Identify the parasite.
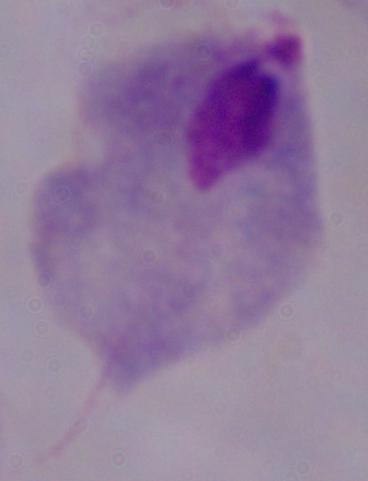
This is a trichomonad.

Micrograph. Captured at 1000x magnification.